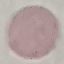

Malaria status: uninfected. Cell patch, automatically extracted from a larger field of view and resized to 64 × 64 pixels. Photographed with a smartphone camera at the microscope eyepiece. Giemsa-stained preparation. Thin blood film.